Locate platelets.
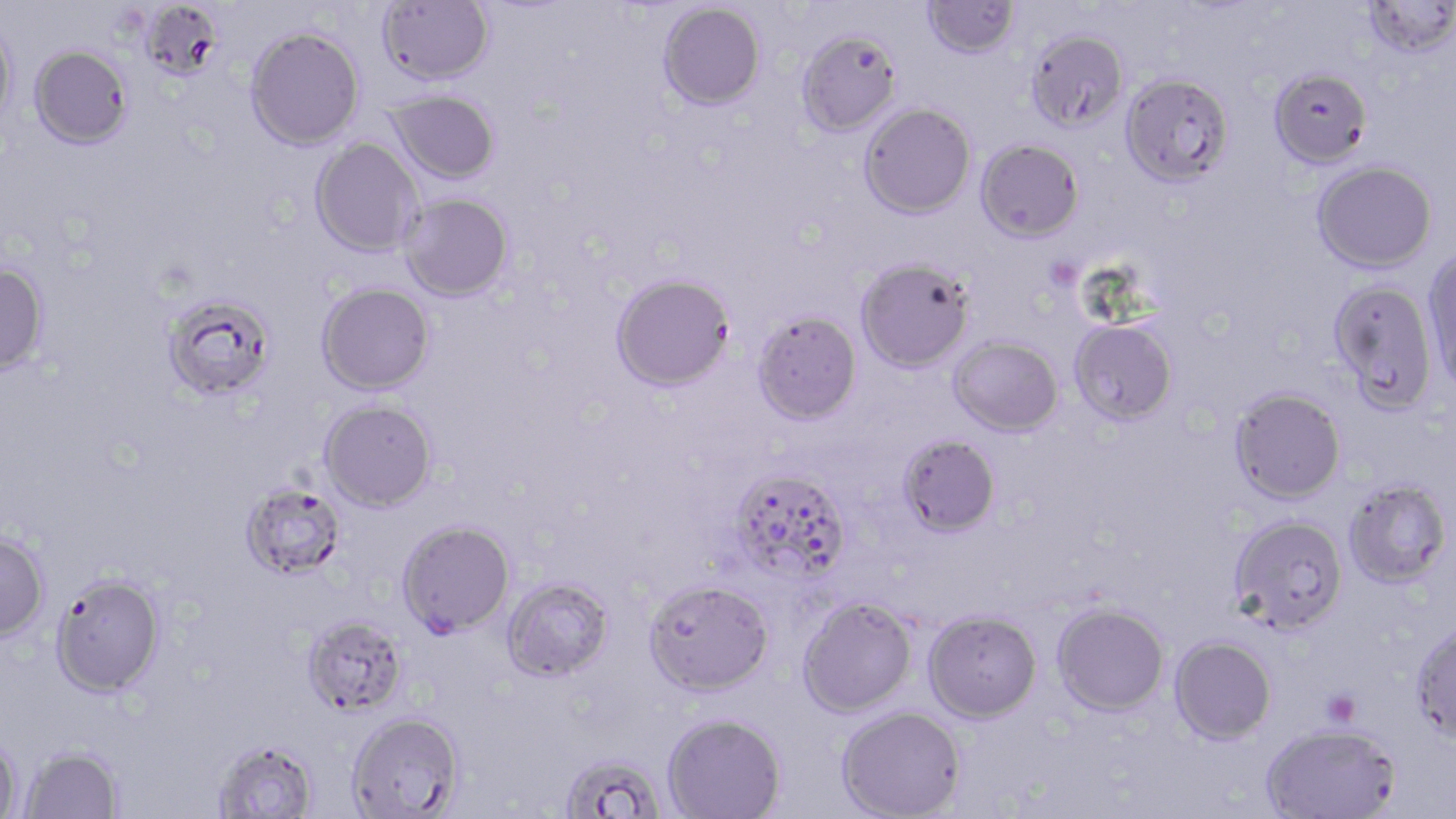
Approximate bounding boxes as [x1, y1, x2, y2] in pixels.
Platelets: [1050, 263, 1081, 289], [1322, 690, 1361, 727].

Summary:
  - Uninfected red blood cell locations: [922, 0, 1020, 59], [1363, 0, 1455, 59], [378, 1, 494, 85], [658, 2, 765, 111], [141, 7, 224, 85], [0, 18, 16, 131], [245, 26, 365, 150], [796, 29, 902, 136], [1026, 29, 1129, 133], [29, 45, 133, 149], [1269, 66, 1373, 168], [1120, 72, 1235, 187], [386, 90, 500, 184], [858, 102, 976, 219], [310, 138, 423, 258], [976, 138, 1084, 242], [1312, 160, 1437, 273], [399, 193, 514, 301], [1422, 247, 1456, 390], [855, 257, 975, 372], [0, 262, 50, 376], [610, 273, 735, 392], [1327, 279, 1438, 413], [316, 282, 435, 395], [161, 292, 278, 403], [752, 311, 862, 425], [1069, 319, 1178, 426], [949, 336, 1063, 436], [1229, 387, 1347, 504], [319, 399, 437, 512], [898, 434, 1001, 537], [727, 467, 851, 585], [1343, 478, 1453, 588], [240, 482, 346, 581], [1228, 514, 1349, 634], [396, 519, 516, 639], [0, 533, 49, 641], [49, 571, 166, 698], [501, 576, 614, 682], [643, 579, 773, 696], [797, 595, 917, 718], [1052, 602, 1169, 716], [923, 609, 1042, 723], [301, 615, 409, 718], [1410, 623, 1456, 744], [1169, 636, 1277, 744], [836, 705, 965, 818], [347, 711, 464, 818], [662, 712, 787, 818], [1260, 722, 1401, 819], [0, 735, 21, 819], [212, 739, 319, 818], [19, 745, 124, 818], [558, 752, 668, 817]
  - Slide-level diagnosis: Plasmodium falciparum
  - Preparation: thin blood film
  - Modality: optical microscopy
  - Stain: May-Grünwald-Giemsa
  - Image size: 1456×819 pixels
  - Magnification: 1000x
  - Field of view: single